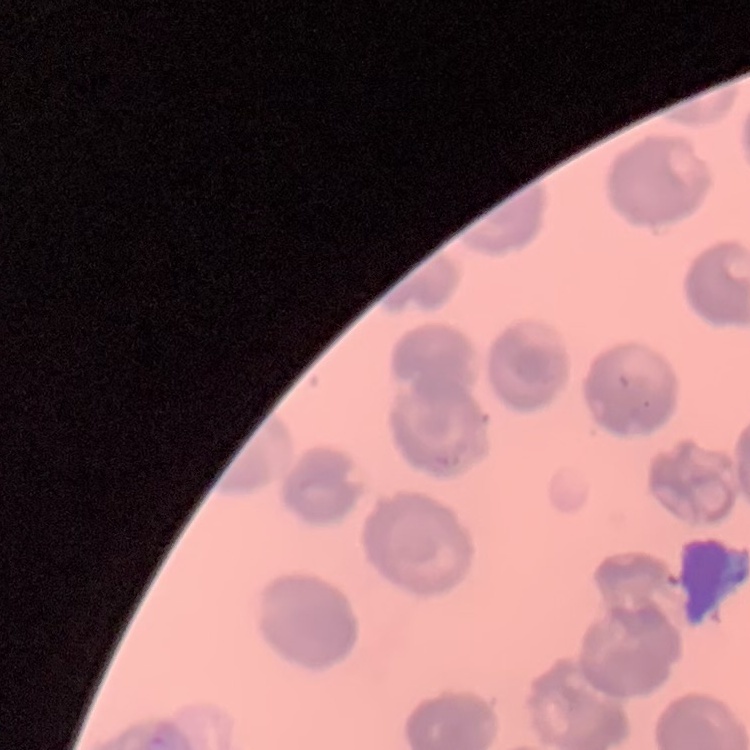

The erythrocytes exhibit no rouleaux formation. Square crop of a larger photomicrograph. Field's or Giemsa stain. Thin blood film.